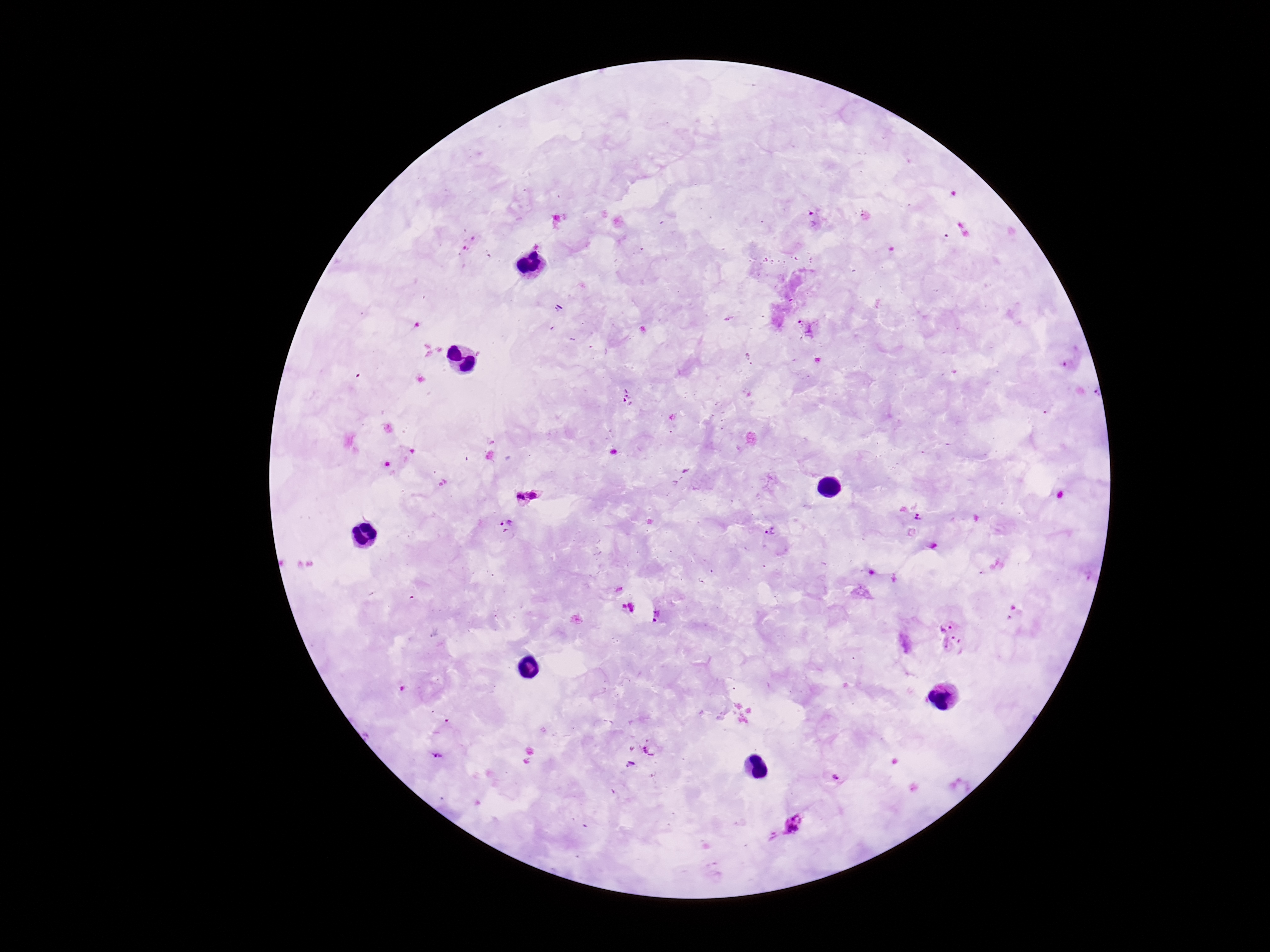
image size = 1270×952 pixels
magnification = 100x
capture = smartphone camera through the microscope eyepiece
field of view = single
stain = Giemsa
Plasmodium parasite locations = approximate centers as (x, y) in pixels: (815, 219), (805, 327), (750, 359), (627, 396), (535, 494), (521, 498), (919, 517), (503, 527), (774, 539), (628, 607), (658, 616), (953, 638), (650, 747), (437, 755), (832, 777), (791, 825)
patient malaria status = infected
preparation = thick blood film